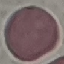
{
  "malaria_status": "uninfected",
  "image_type": "cell patch, automatically extracted from a larger field of view and resized to 64 × 64 pixels",
  "capture": "smartphone through the microscope eyepiece",
  "preparation": "thin blood film",
  "stain": "Giemsa"
}